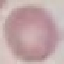 Malaria status: uninfected. Thin blood film. Giemsa-stained preparation. Photographed with a smartphone camera at the microscope eyepiece. Cell patch, automatically extracted from a larger field of view and resized to 64 × 64 pixels.